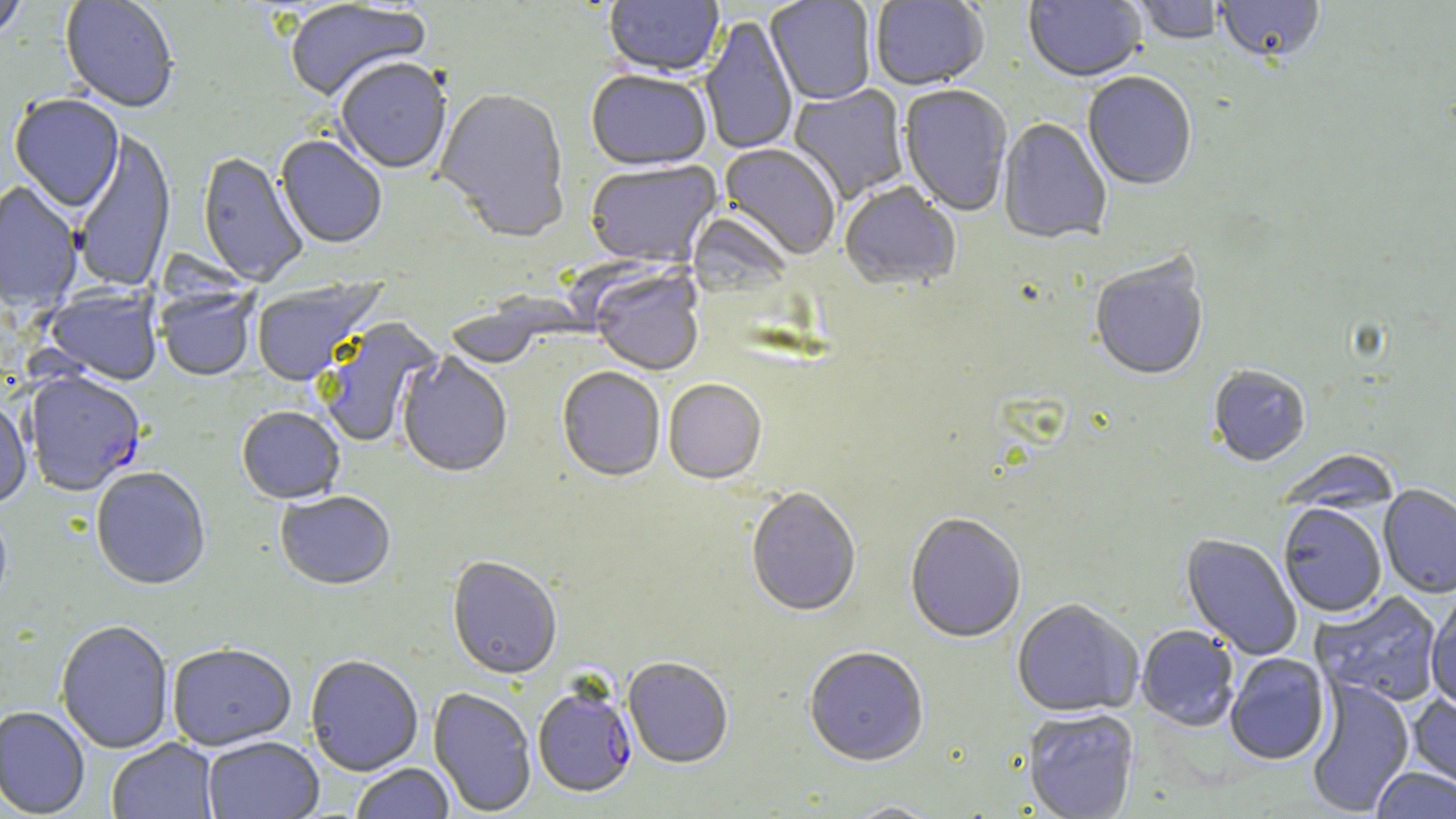 Approximate bounding boxes as (x1, y1, x2, y2) in pixels. Plasmodium falciparum-infected red blood cell locations: (23, 374, 145, 499), (533, 686, 637, 799). Uninfected red blood cell locations: (0, 0, 28, 43), (60, 0, 179, 115), (603, 0, 724, 80), (765, 0, 876, 106), (1023, 0, 1146, 84), (1133, 0, 1224, 47), (1214, 0, 1326, 66), (284, 1, 432, 105), (870, 1, 989, 92), (700, 17, 798, 155), (335, 61, 452, 176), (586, 72, 712, 174), (1082, 74, 1196, 192), (789, 84, 909, 204), (898, 85, 1013, 218), (433, 89, 572, 246), (9, 96, 124, 214), (997, 119, 1111, 246), (72, 130, 177, 294), (274, 135, 387, 250), (718, 145, 840, 261), (197, 152, 308, 288), (585, 161, 723, 270), (0, 182, 83, 315), (839, 184, 961, 293), (1090, 257, 1209, 384), (588, 267, 704, 378), (251, 278, 384, 388), (43, 286, 163, 388), (157, 287, 259, 383), (443, 302, 554, 371), (317, 318, 442, 448), (396, 354, 512, 480), (1208, 366, 1310, 468), (556, 369, 665, 484), (663, 381, 767, 486), (0, 400, 31, 510), (237, 408, 345, 506), (1277, 450, 1400, 515), (91, 469, 211, 592), (1378, 485, 1456, 598), (746, 489, 861, 619), (275, 492, 396, 592), (1279, 504, 1386, 618), (905, 515, 1026, 644), (1180, 533, 1302, 660), (446, 558, 562, 682), (1311, 591, 1442, 708), (1426, 592, 1456, 713), (1012, 600, 1143, 718), (56, 622, 173, 755), (1136, 625, 1239, 732), (167, 645, 297, 752), (804, 648, 929, 768), (1225, 654, 1330, 766), (305, 656, 423, 777), (623, 658, 733, 770), (1306, 679, 1414, 817), (428, 688, 537, 817), (1408, 695, 1456, 797), (0, 708, 91, 818), (1023, 708, 1140, 819), (203, 737, 324, 819), (107, 739, 219, 819), (350, 764, 454, 819), (1371, 768, 1456, 819), (841, 802, 945, 818). Slide-level diagnosis: Plasmodium falciparum. Thin blood film. Image is 1456×819 pixels. May-Grünwald-Giemsa stain. One field of a larger specimen. Light microscopy. 1000x magnification.